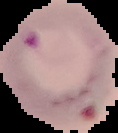
Malaria status: parasitized. Cell region segmented out of the field of view; the surrounding area is masked to black. From a thin blood film. Image is 118×133 pixels.